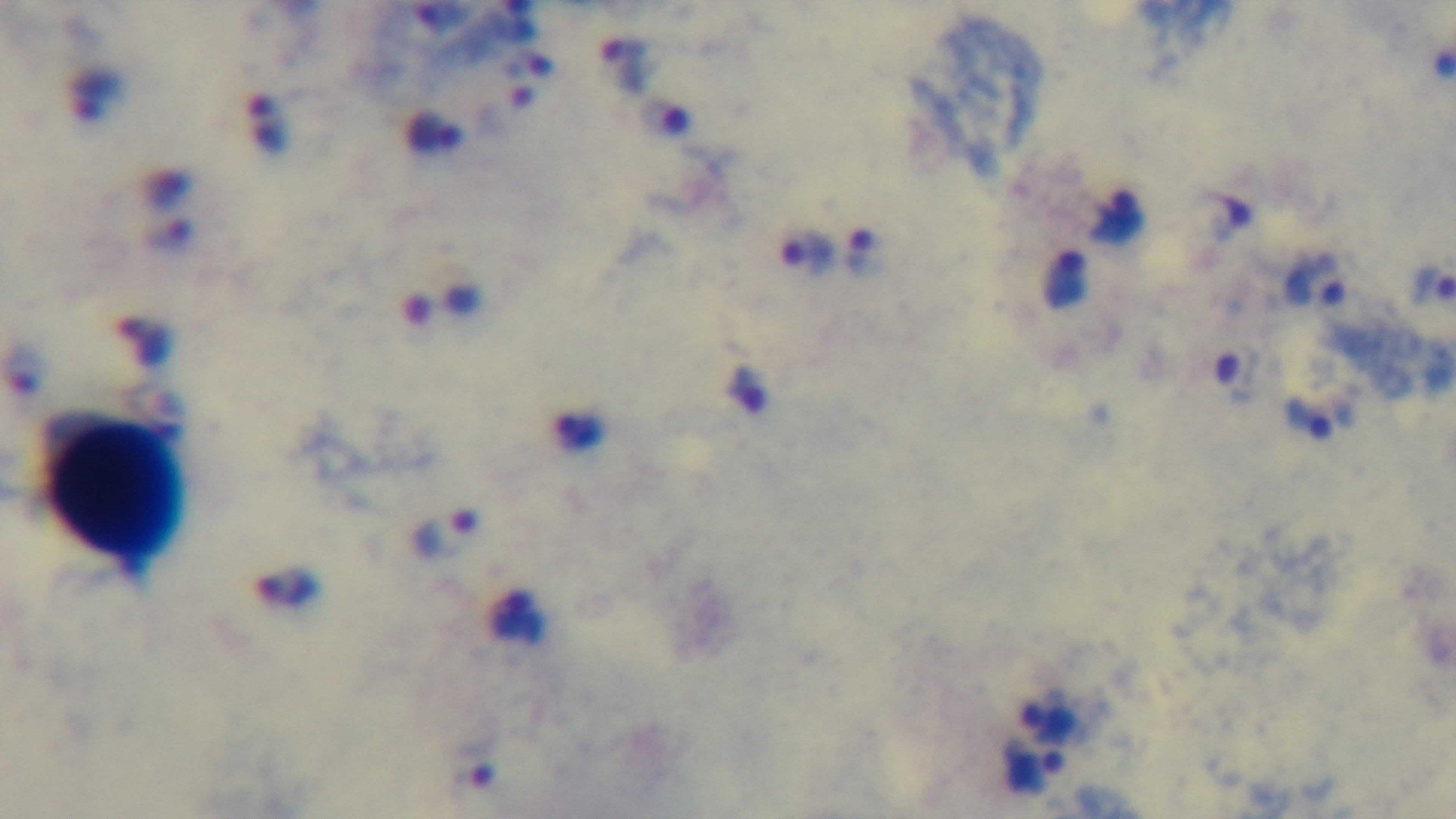

Mounted 4K digital camera. Preparation: thick smear. One field from the slide. Photomicrograph. Oil-immersion objective, 100x. Malaria status: infected. Giemsa stain.